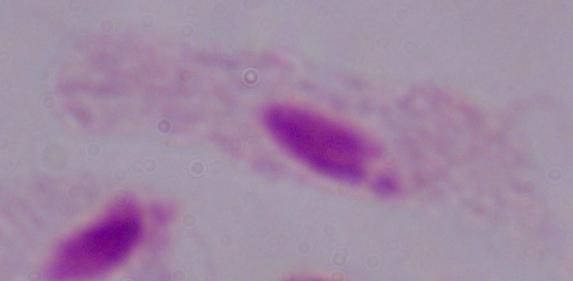
{
  "magnification": "1000x",
  "identification": "trichomonad",
  "modality": "photomicrograph"
}